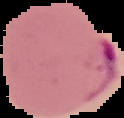

Malaria status: parasitized. Cell region segmented out of the field of view; the surrounding area is masked to black. Image is 124×118 pixels. From a thin blood film.